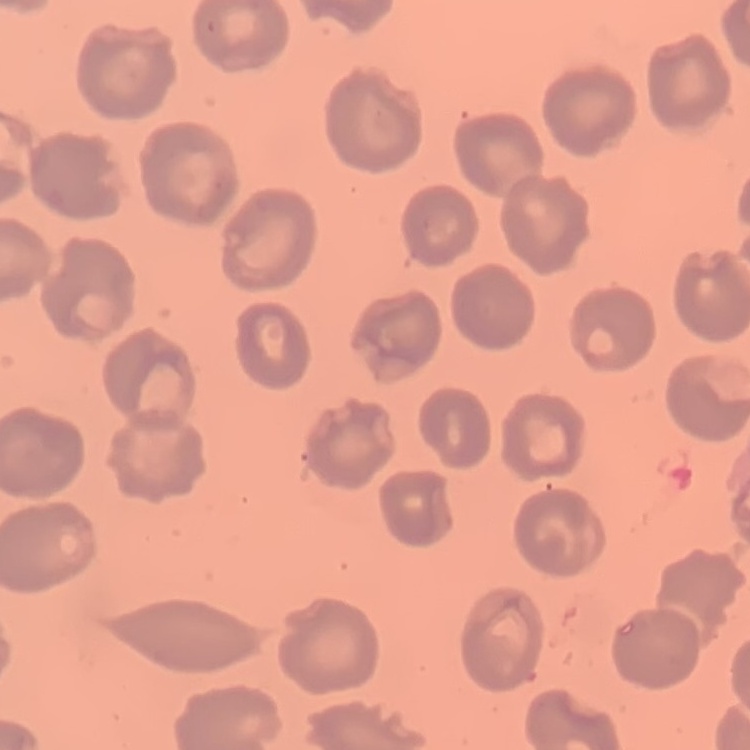
Summary:
  - Red blood cell morphology: no rouleaux formation
  - Image type: square crop of a larger photomicrograph
  - Stain: Field's or Giemsa
  - Preparation: thin peripheral smear